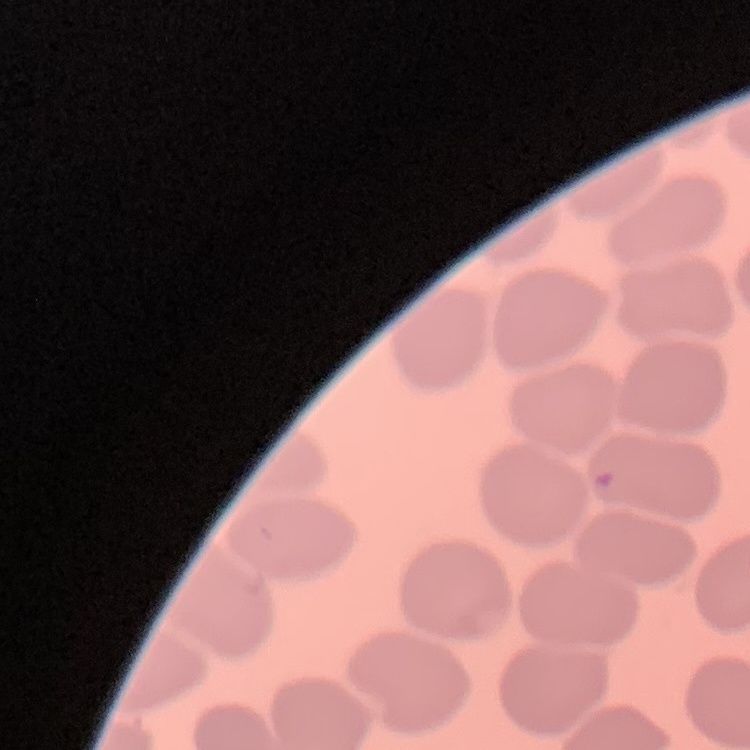
The red blood cells exhibit no rouleaux formation. Thin peripheral smear. One tile cut from a larger photomicrograph. Stained with either Field's or Giemsa.